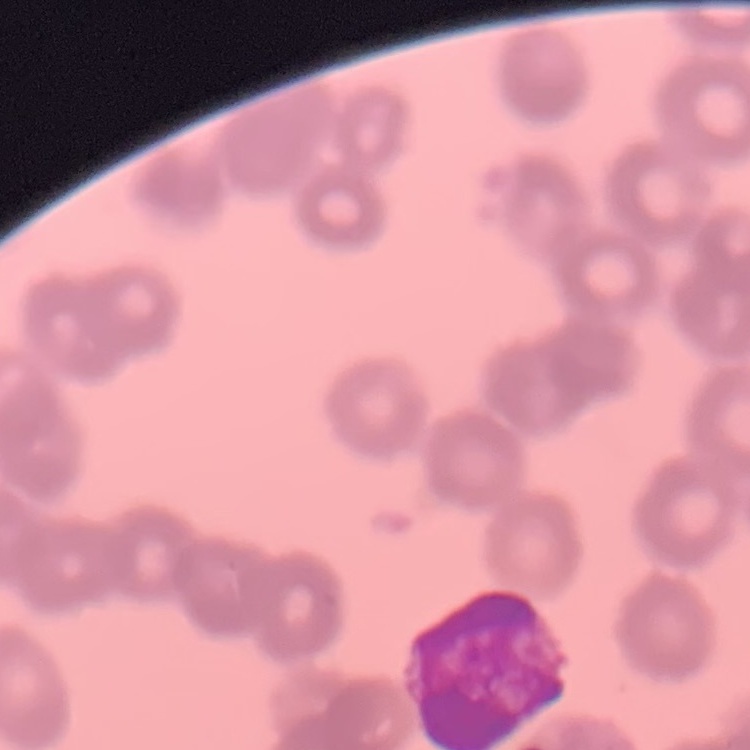 The erythrocytes exhibit rouleaux formation. Field's or Giemsa stain. Square crop of a larger photomicrograph. Thin blood smear.